Give the position of every malaria parasite.
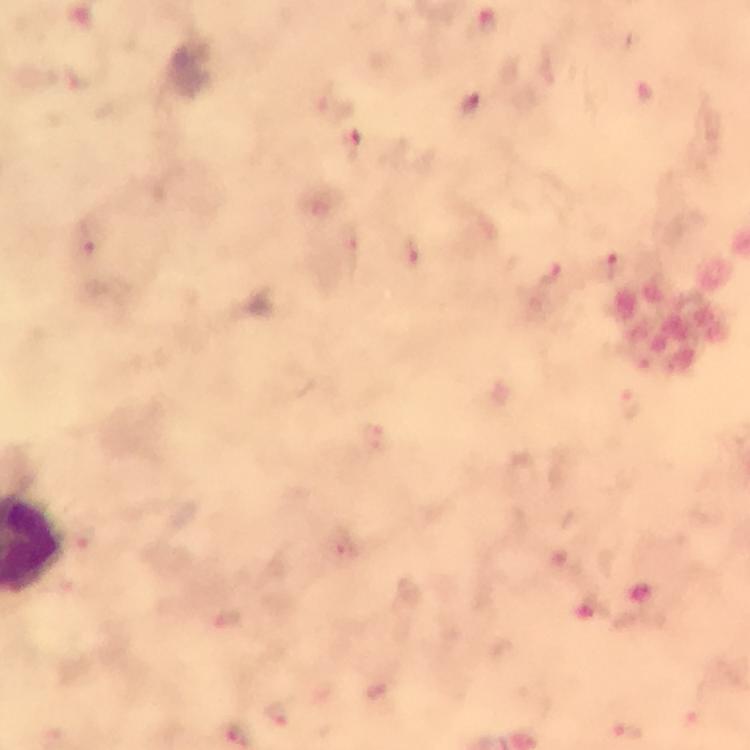

Approximate object centers, in pixels from the top-left corner.
Malaria parasites: (x=471, y=105), (x=413, y=253), (x=614, y=267), (x=551, y=274), (x=628, y=733).

Summary:
  - Image size: 750×750 pixels
  - Context: from a malaria diagnostic workup
  - Capture: smartphone camera through the microscope
  - Magnification: 100x
  - Preparation: thick blood smear
  - Stain: Giemsa
  - Cropped from: one field of view
  - Immersion oil: used